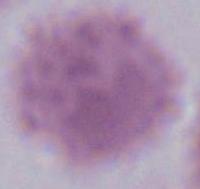
Summary:
  - Magnification: 1000x
  - Modality: photomicrograph
  - Identification: red blood cell